Comment on the morphology of the erythrocytes.
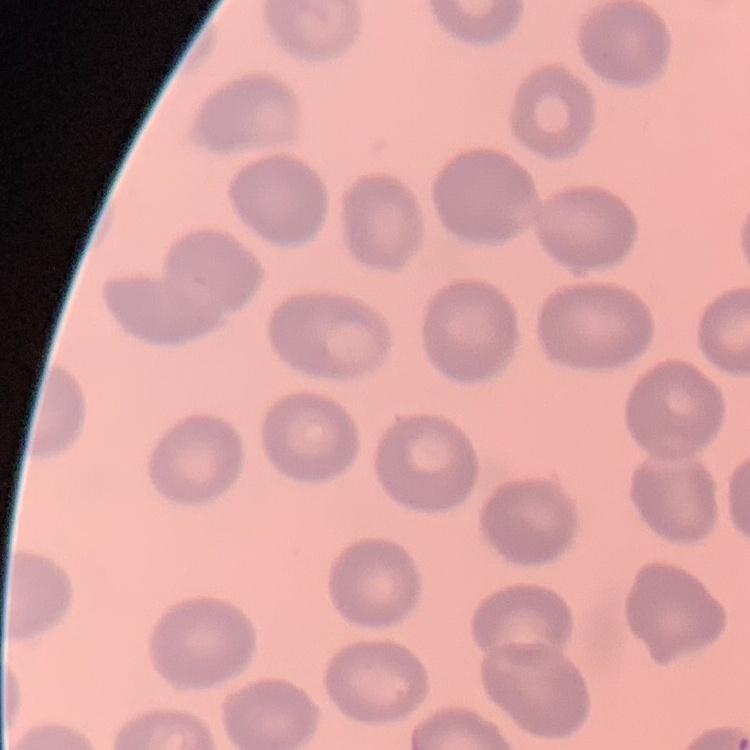
They show no rouleaux formation.

{
  "preparation": "thin blood smear",
  "stain": "Field's or Giemsa",
  "image_type": "one tile cut from a larger photomicrograph"
}